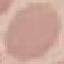 Result: no malaria parasites detected. Thin blood film. Giemsa-stained preparation. Automatically extracted cell patch, resized to 64 × 64 pixels. Acquired by smartphone through the microscope eyepiece.